Classify this cell by malaria status.
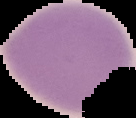
It is uninfected.

{
  "image_size": "136×118 pixels",
  "preparation": "thin blood smear",
  "image_type": "segmented cell region on a black background"
}